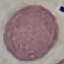

result: no malaria parasites detected
preparation: thin smear
capture: smartphone camera at the microscope eyepiece
image_type: cell patch, automatically extracted from a larger field of view and resized to 64 × 64 pixels
stain: Giemsa